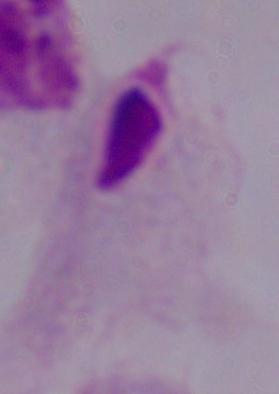
Summary:
  - Identification: trichomonad
  - Magnification: 1000x
  - Modality: photomicrograph